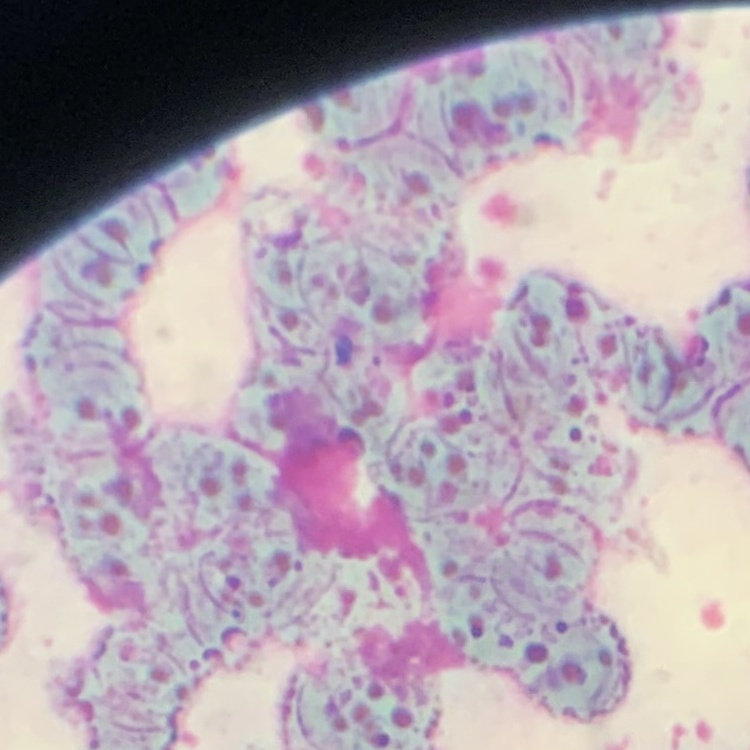

Summary:
  - Erythrocyte morphology: rouleaux formation
  - Image type: square crop of a larger photomicrograph
  - Stain: Field's or Giemsa
  - Preparation: thin peripheral smear